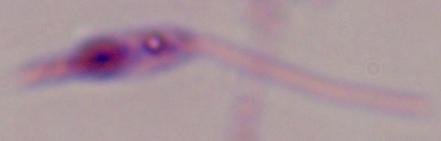
Summary:
  - Modality: micrograph
  - Identification: Leishmania
  - Magnification: 1000x